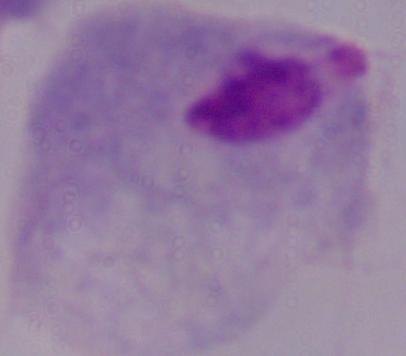
magnification: 1000x
identification: trichomonad
modality: micrograph